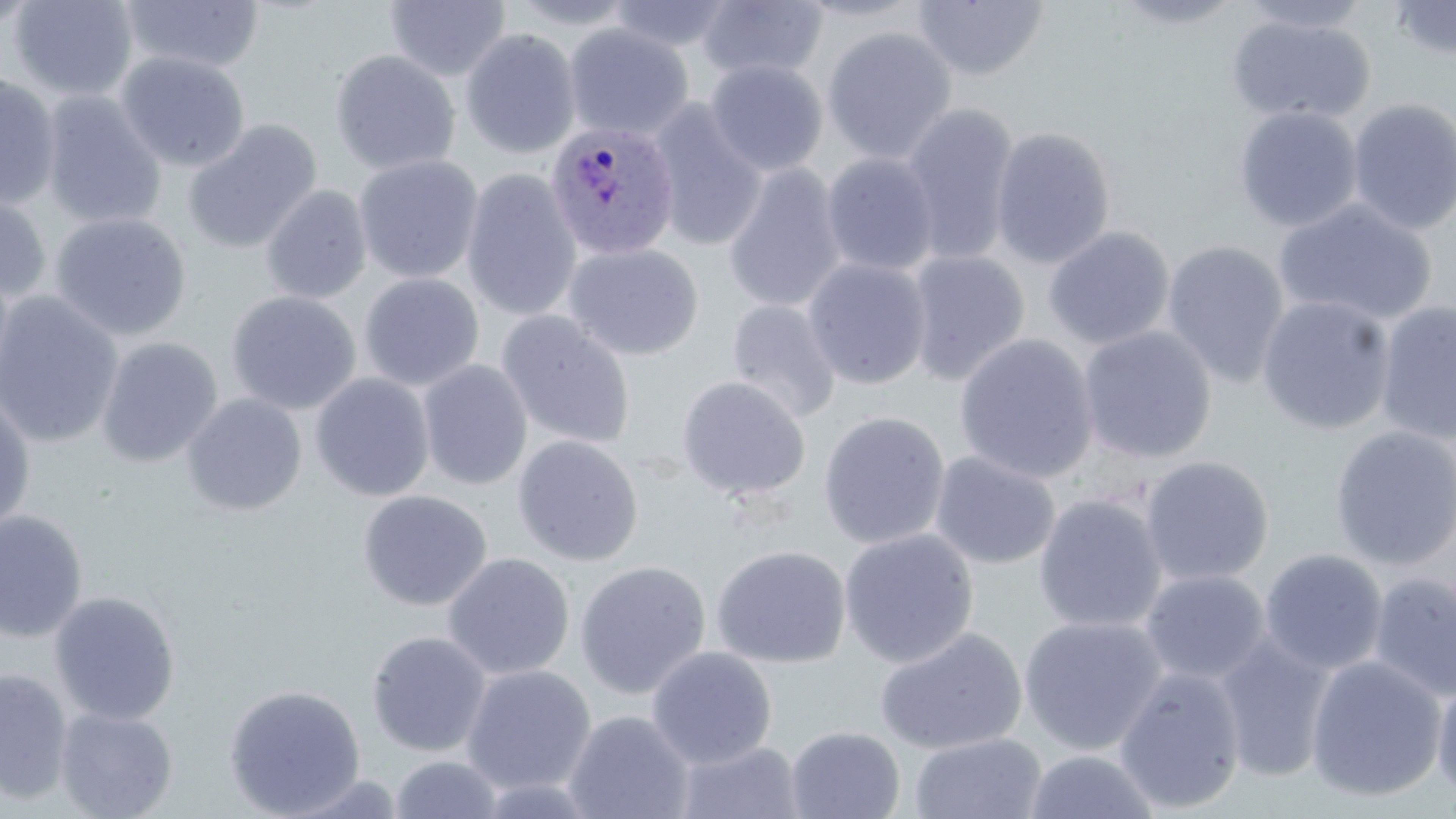

{
  "slide_level_diagnosis": "Plasmodium ovale",
  "stain": "May-Grünwald-Giemsa",
  "modality": "light microscopy",
  "image_size": "1456×819 pixels",
  "magnification": "1000x",
  "plasmodium_ovale_infected_red_blood_cell_locations": "approximate bounding boxes as named x1/y1/x2/y2 corners in pixels: (x1=545, y1=121, x2=681, y2=261)",
  "field_of_view": "one of a larger specimen",
  "preparation": "thin blood film",
  "uninfected_red_blood_cell_locations": "approximate bounding boxes as named x1/y1/x2/y2 corners in pixels: (x1=8, y1=0, x2=139, y2=102), (x1=383, y1=0, x2=512, y2=83), (x1=505, y1=0, x2=641, y2=30), (x1=792, y1=0, x2=927, y2=22), (x1=1106, y1=0, x2=1250, y2=30), (x1=1232, y1=0, x2=1376, y2=34), (x1=1387, y1=0, x2=1456, y2=63), (x1=0, y1=1, x2=40, y2=36), (x1=120, y1=1, x2=265, y2=74), (x1=606, y1=1, x2=734, y2=54), (x1=695, y1=1, x2=828, y2=83), (x1=911, y1=1, x2=1050, y2=81), (x1=1227, y1=13, x2=1375, y2=125), (x1=564, y1=24, x2=693, y2=141), (x1=821, y1=26, x2=958, y2=165), (x1=460, y1=29, x2=582, y2=159), (x1=329, y1=49, x2=460, y2=176), (x1=116, y1=52, x2=251, y2=172), (x1=705, y1=59, x2=828, y2=176), (x1=0, y1=74, x2=62, y2=210), (x1=39, y1=91, x2=167, y2=231), (x1=1346, y1=97, x2=1456, y2=236), (x1=646, y1=100, x2=767, y2=252), (x1=899, y1=102, x2=1021, y2=266), (x1=1234, y1=105, x2=1363, y2=233), (x1=183, y1=120, x2=322, y2=254), (x1=990, y1=125, x2=1116, y2=269), (x1=821, y1=152, x2=941, y2=277), (x1=354, y1=155, x2=484, y2=284), (x1=721, y1=162, x2=847, y2=314), (x1=461, y1=170, x2=582, y2=323), (x1=260, y1=185, x2=372, y2=304), (x1=0, y1=191, x2=52, y2=304), (x1=1274, y1=199, x2=1438, y2=327), (x1=50, y1=212, x2=192, y2=341), (x1=1043, y1=226, x2=1175, y2=350), (x1=1161, y1=240, x2=1290, y2=388), (x1=563, y1=243, x2=704, y2=361), (x1=905, y1=249, x2=1031, y2=387), (x1=803, y1=258, x2=932, y2=390), (x1=358, y1=273, x2=484, y2=391), (x1=226, y1=290, x2=361, y2=415), (x1=0, y1=292, x2=124, y2=449), (x1=1256, y1=295, x2=1396, y2=435), (x1=726, y1=298, x2=842, y2=424), (x1=1374, y1=299, x2=1456, y2=445), (x1=496, y1=310, x2=635, y2=450), (x1=1076, y1=325, x2=1217, y2=465), (x1=954, y1=332, x2=1099, y2=485), (x1=96, y1=337, x2=222, y2=468), (x1=418, y1=359, x2=533, y2=491), (x1=310, y1=373, x2=435, y2=502), (x1=676, y1=376, x2=812, y2=503), (x1=0, y1=392, x2=36, y2=534), (x1=181, y1=393, x2=307, y2=517), (x1=818, y1=411, x2=950, y2=550), (x1=1328, y1=425, x2=1456, y2=571), (x1=512, y1=435, x2=643, y2=567), (x1=929, y1=451, x2=1060, y2=570), (x1=1140, y1=455, x2=1275, y2=587), (x1=358, y1=489, x2=492, y2=611), (x1=1033, y1=494, x2=1168, y2=634), (x1=0, y1=509, x2=88, y2=643), (x1=839, y1=528, x2=979, y2=668), (x1=711, y1=545, x2=850, y2=668), (x1=1259, y1=549, x2=1388, y2=676), (x1=442, y1=552, x2=575, y2=681), (x1=574, y1=560, x2=711, y2=700), (x1=1140, y1=569, x2=1270, y2=686), (x1=1367, y1=570, x2=1456, y2=703), (x1=49, y1=590, x2=181, y2=725), (x1=1018, y1=615, x2=1168, y2=756), (x1=874, y1=627, x2=1026, y2=755), (x1=366, y1=631, x2=492, y2=757), (x1=1212, y1=632, x2=1338, y2=784), (x1=646, y1=646, x2=778, y2=769), (x1=1305, y1=655, x2=1448, y2=803), (x1=461, y1=664, x2=597, y2=795), (x1=0, y1=666, x2=73, y2=806), (x1=1113, y1=666, x2=1247, y2=814), (x1=1431, y1=674, x2=1456, y2=805), (x1=224, y1=683, x2=366, y2=817), (x1=55, y1=707, x2=177, y2=819), (x1=564, y1=709, x2=694, y2=819), (x1=785, y1=726, x2=905, y2=819), (x1=908, y1=732, x2=1048, y2=819), (x1=675, y1=739, x2=805, y2=819), (x1=1022, y1=748, x2=1164, y2=819), (x1=388, y1=754, x2=505, y2=818)"
}